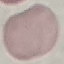

Summary:
  - Result: no malaria parasites seen
  - Stain: Giemsa
  - Image type: automatically extracted cell patch, resized to 64 × 64 pixels
  - Preparation: thin blood film
  - Capture: smartphone camera at the microscope eyepiece